State which cell type is depicted.
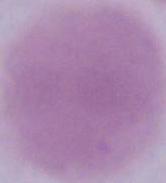

This is an erythrocyte.

Captured at 1000x magnification. Photomicrograph.